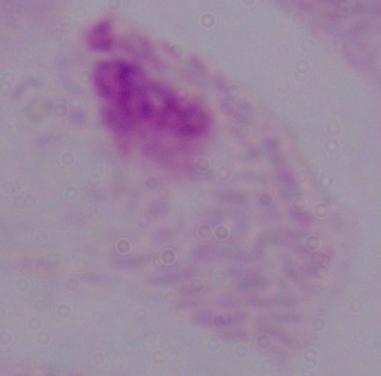
Summary:
  - Magnification: 1000x
  - Modality: photomicrograph
  - Identification: trichomonad